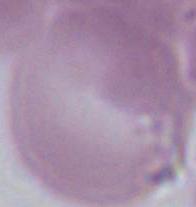
Photomicrograph. An erythrocyte is seen. Captured at 1000x magnification.